Identify the cell.
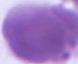

This is an erythrocyte.

modality: photomicrograph
magnification: 1000x